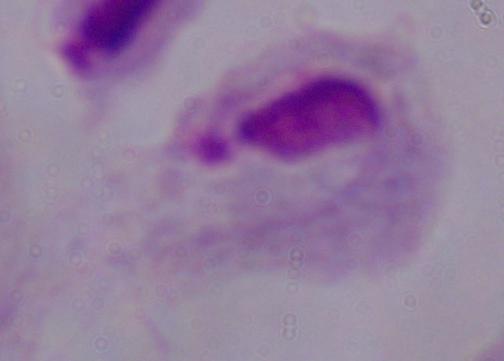

Summary:
  - Magnification: 1000x
  - Identification: trichomonad
  - Modality: photomicrograph